Report the malaria status of this cell.
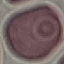

It is uninfected.

Summary:
  - Capture: smartphone camera at the microscope eyepiece
  - Stain: Giemsa
  - Preparation: thin blood film
  - Image type: automatically extracted cell patch, resized to 64 × 64 pixels